Report the malaria status of this cell.
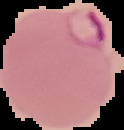

It is parasitized.

preparation = thin blood film
image type = cell region segmented out of the field of view; surrounding area masked to black
image size = 124×130 pixels